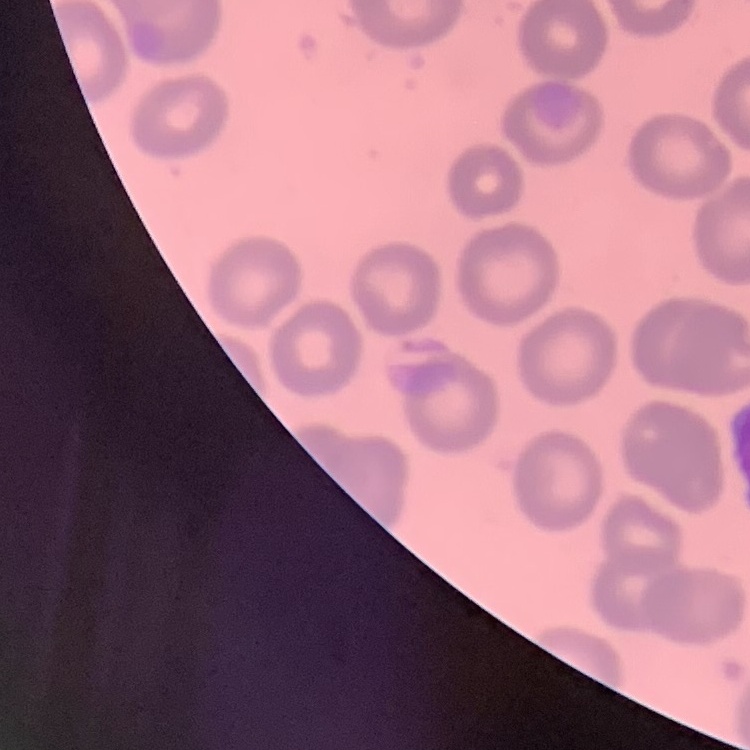
Summary:
  - Erythrocyte morphology: no rouleaux formation
  - Stain: Field's or Giemsa
  - Image type: square crop of a larger photomicrograph
  - Preparation: thin blood film